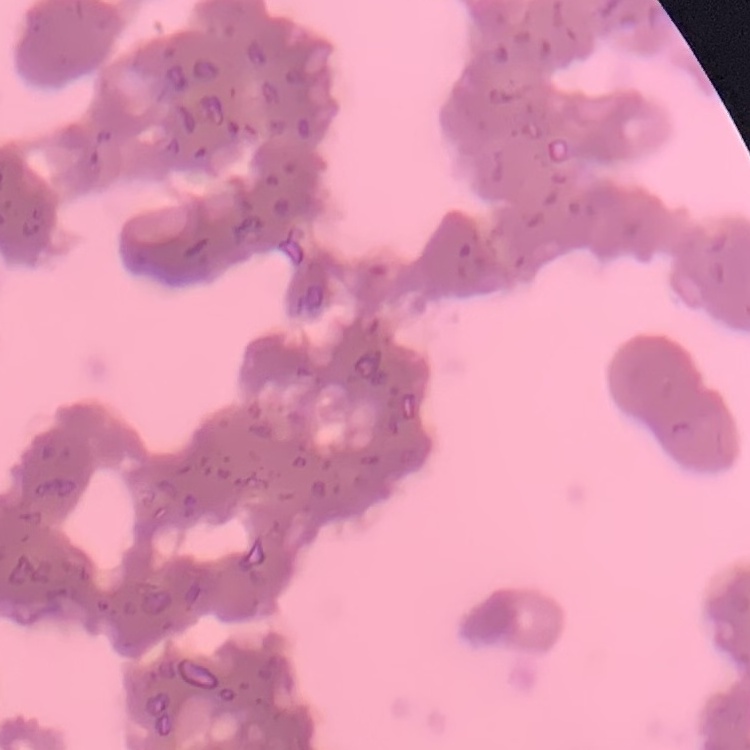

erythrocyte morphology = rouleaux formation
image type = one tile cut from a larger photomicrograph
preparation = thin blood film
stain = Field's or Giemsa